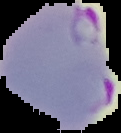
Summary:
  - Image size: 121×133 pixels
  - Preparation: thin blood film
  - Result: malaria parasites detected
  - Image type: segmented cell region with the area outside set to black